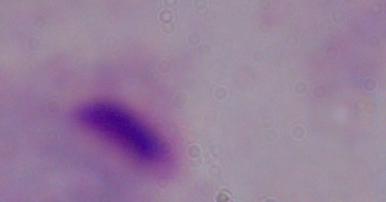
{
  "modality": "photomicrograph",
  "magnification": "1000x",
  "identification": "trichomonad"
}